Comment on the morphology of the red blood cells.
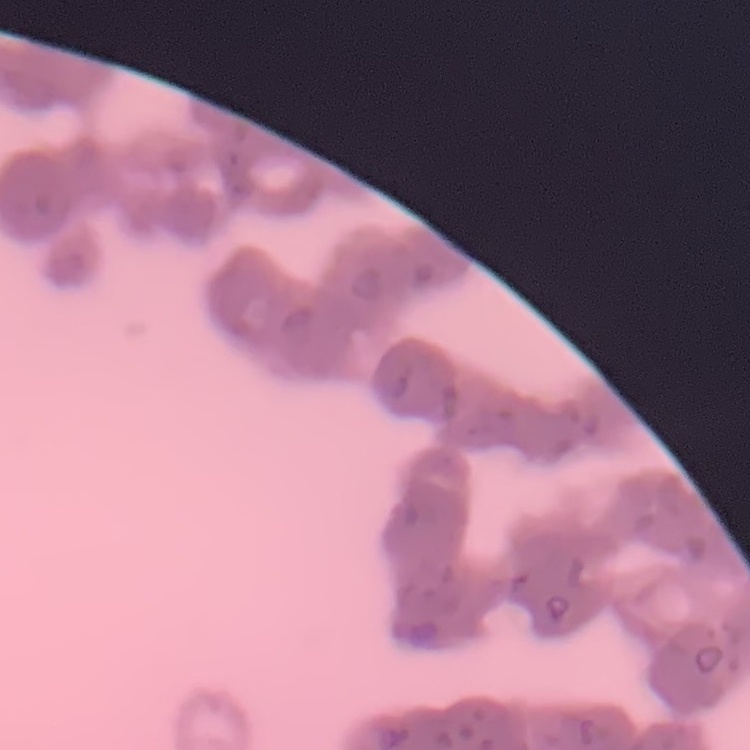
Rouleaux formation.

Summary:
  - Preparation: thin peripheral smear
  - Stain: Field's or Giemsa
  - Image type: one tile cut from a larger photomicrograph